Point out each Plasmodium parasite.
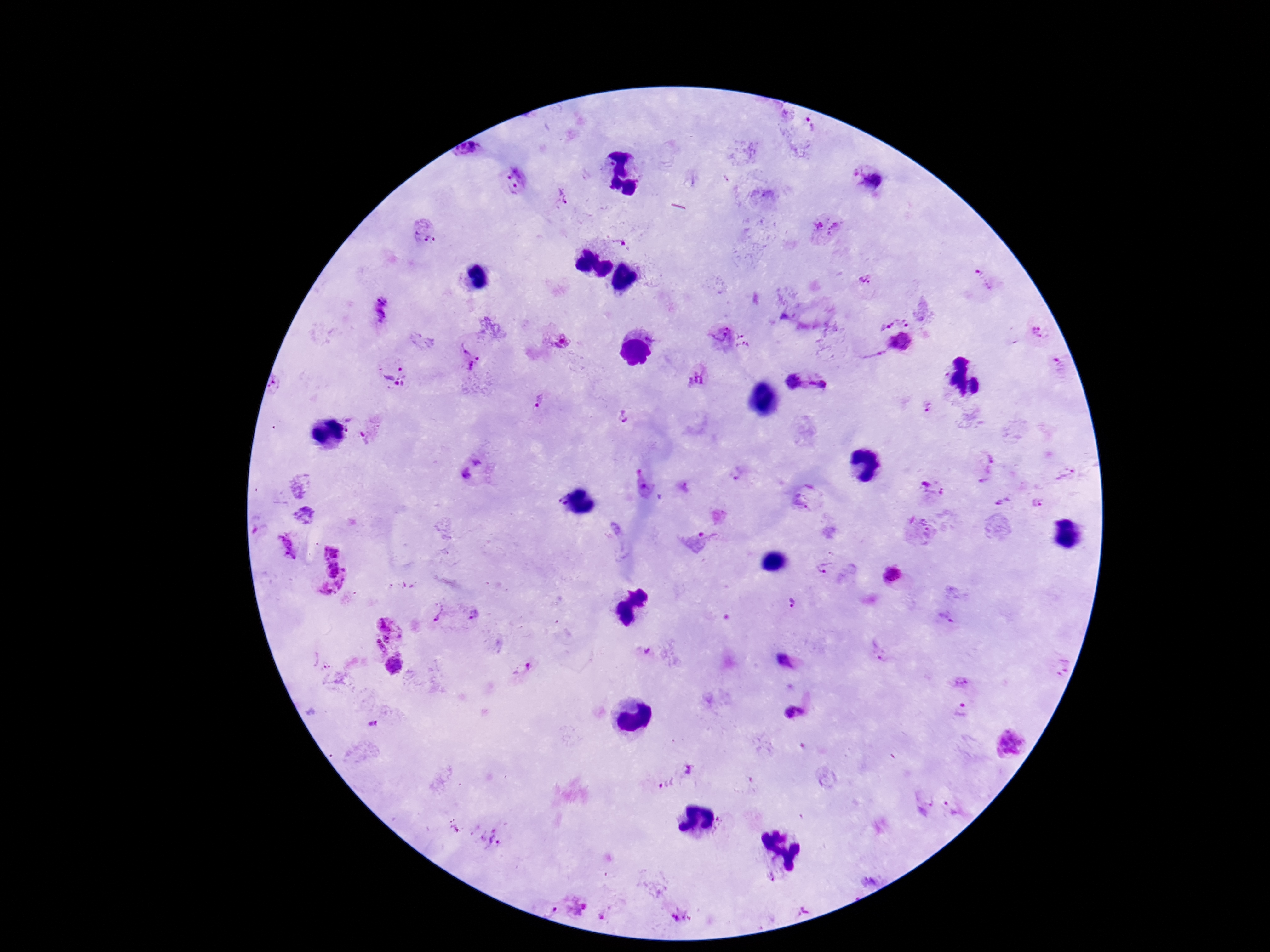
Approximate centers as [x, y] in pixels.
Plasmodium parasites: [806, 131], [470, 150], [870, 178], [516, 180], [562, 196], [823, 227], [426, 232], [619, 240], [984, 280], [865, 281], [380, 311], [905, 321], [888, 326], [1038, 331], [731, 339], [557, 340], [469, 358], [1056, 369], [393, 374], [698, 378], [793, 382], [817, 383], [276, 387], [539, 402], [928, 407], [624, 415], [985, 469], [476, 471], [736, 473], [1066, 475], [684, 487], [932, 490], [804, 498], [557, 501], [1003, 502], [1037, 502], [917, 534], [695, 542], [287, 544], [318, 560], [826, 568], [895, 575], [341, 587], [791, 602], [438, 614], [473, 615], [945, 618], [388, 630], [880, 651], [651, 655], [322, 661], [787, 661], [394, 666], [1059, 666], [522, 670], [958, 683], [962, 710], [793, 711], [372, 725], [1010, 742], [688, 770], [663, 784], [920, 798], [955, 806], [491, 838], [550, 911], [678, 916].

patient malaria status = positive
capture = smartphone camera through the microscope eyepiece
field of view = single
image size = 1270×952 pixels
preparation = thick blood film
magnification = 100x
stain = Giemsa